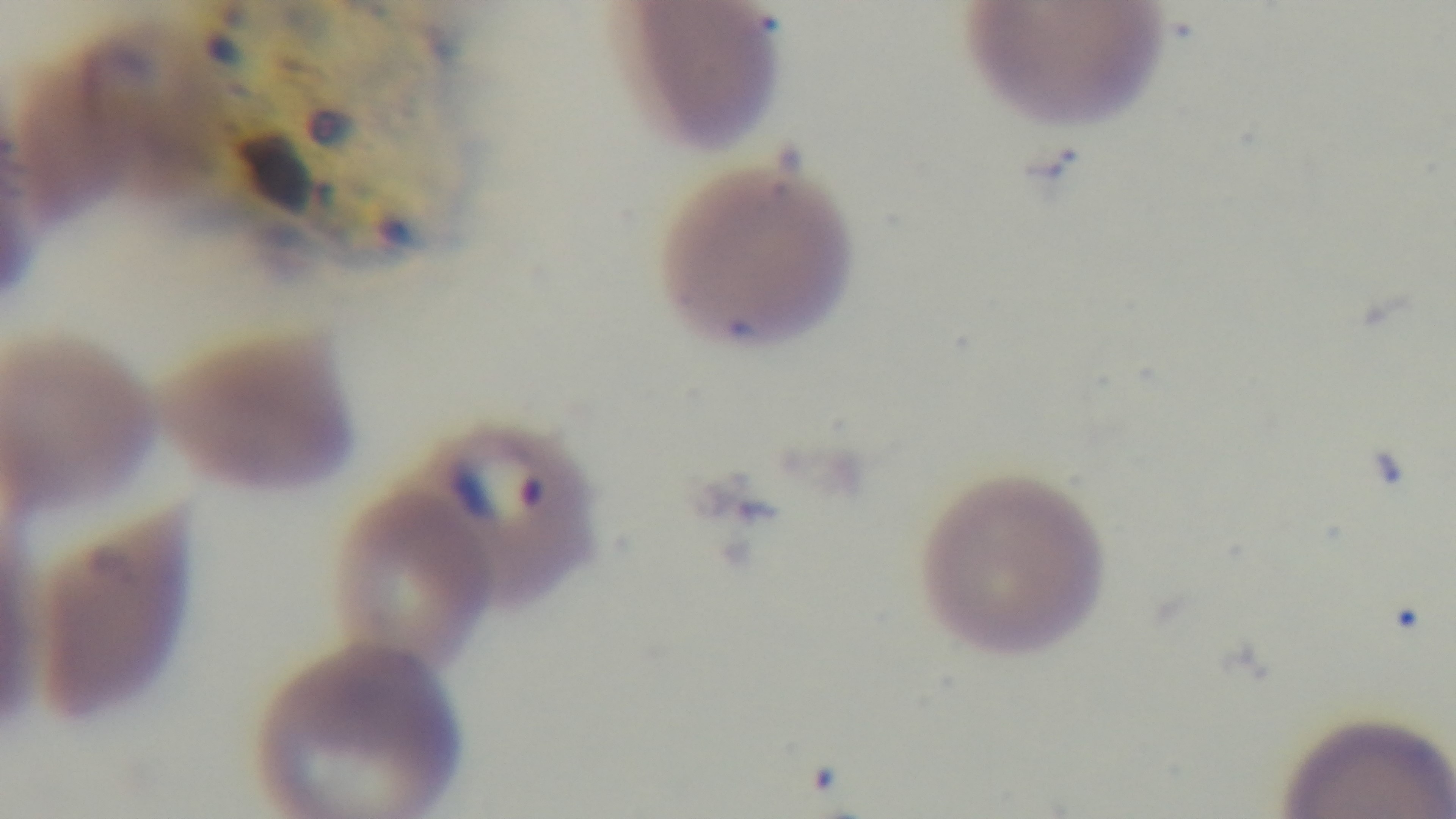 One field from the slide. Preparation: thin. Giemsa-stained. 100x oil-immersion objective. Malaria status: infected. Light microscopy. Mounted 4K digital camera.